Locate every Plasmodium parasite.
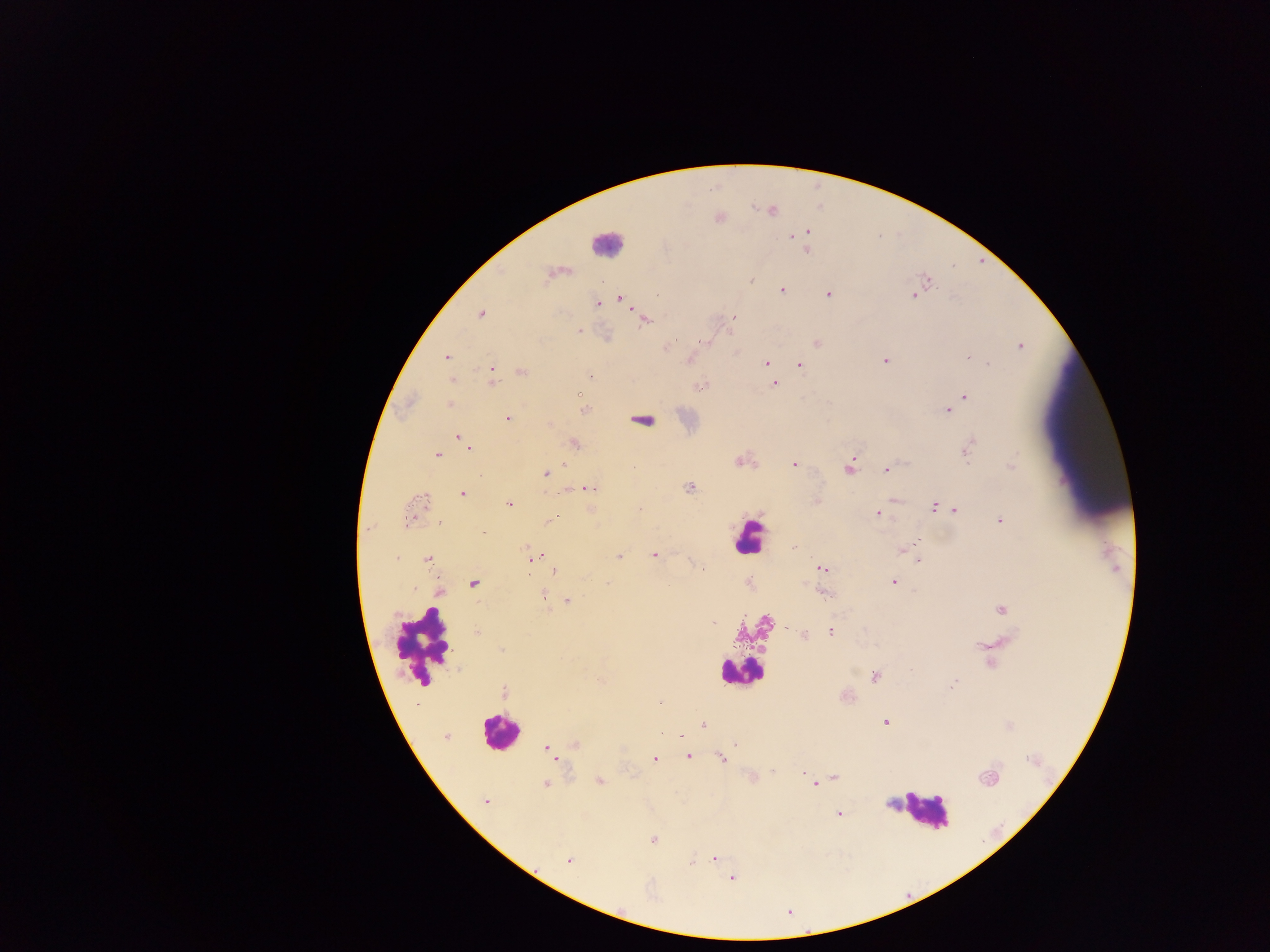
Approximate centers as [x, y] in pixels.
Plasmodium parasites: [772, 211], [718, 217], [805, 231], [799, 232], [792, 234], [804, 250], [556, 272], [750, 279], [927, 280], [781, 289], [828, 294], [914, 295], [620, 298], [597, 303], [480, 314], [733, 316], [644, 318], [578, 330], [607, 336], [703, 342], [816, 343], [1020, 345], [665, 346], [446, 358], [968, 358], [884, 360], [766, 362], [799, 365], [491, 370], [521, 371], [591, 376], [491, 381], [773, 384], [698, 386], [578, 393], [965, 396], [408, 401], [450, 405], [952, 406], [582, 409], [947, 410], [508, 419], [640, 419], [459, 438], [574, 444], [468, 446], [967, 449], [437, 455], [742, 461], [794, 463], [1011, 466], [849, 467], [886, 469], [544, 473], [567, 487], [688, 487], [589, 488], [462, 494], [893, 499], [509, 503], [933, 506], [639, 509], [955, 509], [592, 511], [413, 512], [878, 513], [999, 519], [550, 520], [481, 533], [914, 544], [793, 548], [902, 549], [654, 555], [532, 557], [619, 557], [429, 559], [918, 559], [701, 567], [821, 568], [555, 570], [893, 582], [473, 584], [821, 591], [439, 592], [543, 597], [567, 601], [1001, 609], [712, 622], [476, 631], [830, 631], [805, 635], [875, 676], [952, 684], [504, 692], [845, 695], [886, 722], [702, 724], [1009, 725], [661, 734], [680, 735], [445, 736], [735, 743], [574, 744], [546, 748], [688, 755], [721, 758], [654, 759], [773, 771], [804, 771], [749, 776], [987, 777], [834, 778], [599, 781], [815, 783], [546, 784], [485, 802], [891, 803], [838, 814], [653, 839], [714, 859], [567, 860], [690, 861], [731, 877].

Leukocyte locations: [606, 244], [749, 536], [754, 627], [423, 645], [742, 671], [500, 732], [926, 810]. Thick blood film. Mobile-phone photograph taken through the microscope. Collected in Ghana. One field of view. Image is 1270×952 pixels.